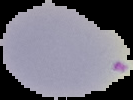

Summary:
  - Image type: cell region segmented out of the field of view; surrounding area masked to black
  - Preparation: thin blood film
  - Result: malaria parasites detected
  - Image size: 133×100 pixels